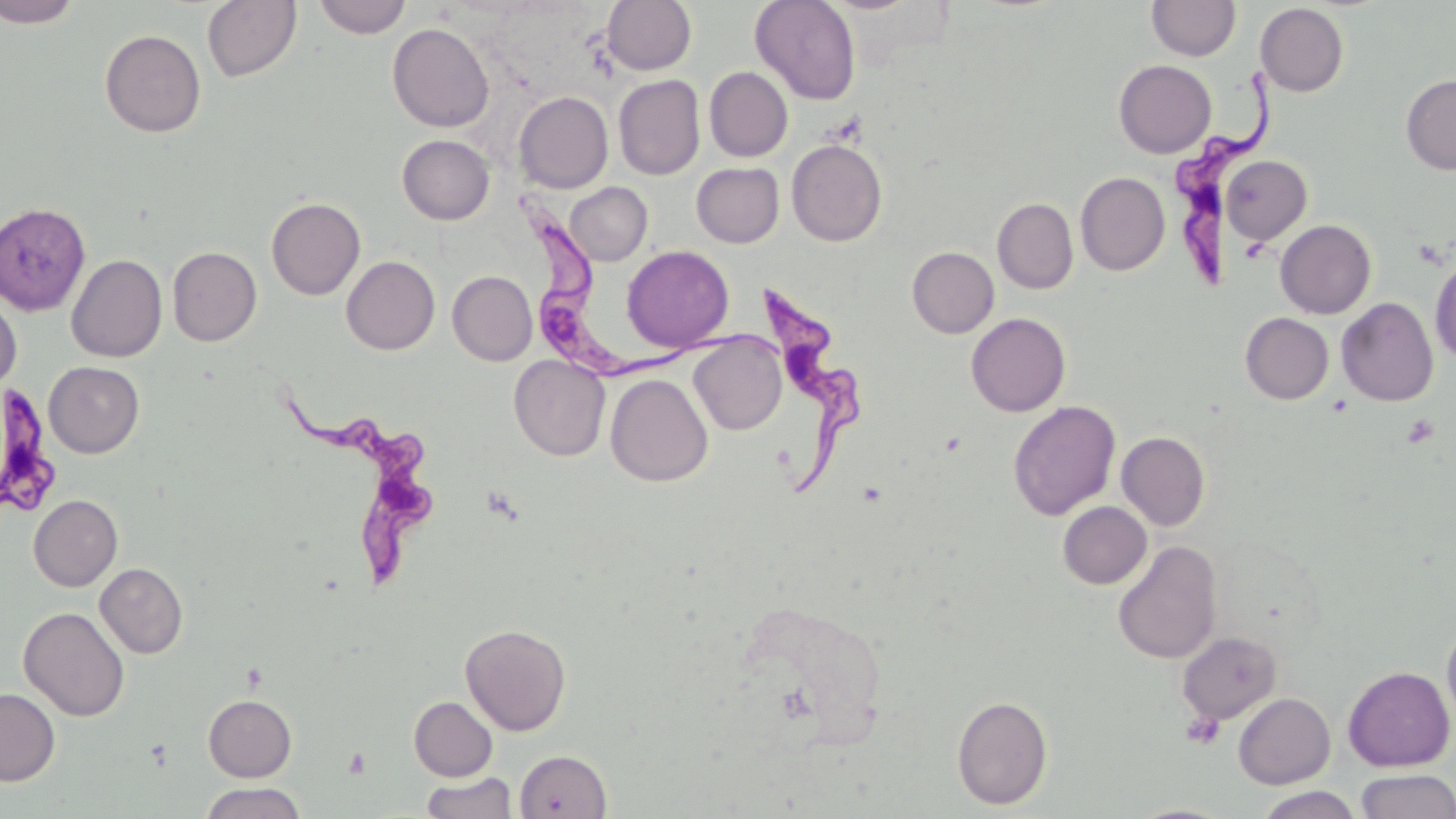

Approximate bounding boxes as [x1, y1, x2, y2] in pixels. Platelet locations: [1401, 414, 1439, 449], [1181, 711, 1223, 751], [344, 747, 371, 779]. Trypanosoma brucei locations: [1169, 73, 1284, 289], [507, 191, 689, 384], [759, 289, 873, 497], [275, 381, 453, 592], [0, 383, 63, 525]. Uninfected red blood cell locations: [1, 0, 84, 28], [312, 0, 412, 38], [601, 0, 696, 75], [749, 0, 861, 105], [201, 1, 302, 82], [1146, 1, 1240, 60], [1255, 3, 1349, 97], [387, 23, 495, 132], [99, 29, 206, 138], [1114, 60, 1216, 158], [704, 67, 793, 162], [1400, 73, 1456, 175], [613, 75, 705, 180], [514, 91, 613, 193], [397, 134, 495, 225], [787, 140, 887, 246], [1221, 155, 1312, 244], [691, 162, 785, 247], [1075, 172, 1170, 275], [565, 182, 652, 266], [266, 197, 365, 300], [993, 198, 1078, 294], [0, 203, 91, 316], [1275, 219, 1376, 319], [621, 245, 734, 353], [167, 246, 262, 346], [907, 246, 999, 338], [66, 254, 167, 362], [341, 256, 440, 355], [1430, 256, 1456, 362], [447, 271, 537, 366], [0, 290, 22, 392], [1336, 297, 1439, 406], [966, 313, 1071, 416], [1240, 313, 1333, 404], [688, 331, 787, 435], [509, 354, 610, 460], [44, 361, 144, 458], [605, 374, 713, 487], [1008, 400, 1121, 521], [1117, 431, 1211, 530], [29, 494, 122, 591], [1057, 501, 1152, 589], [1113, 540, 1223, 664], [95, 563, 188, 658], [739, 598, 891, 745], [19, 606, 130, 721], [1442, 621, 1456, 727], [460, 623, 571, 735], [1177, 631, 1282, 724], [1343, 666, 1454, 771], [0, 688, 60, 785], [1233, 693, 1335, 789], [203, 694, 297, 782], [951, 695, 1053, 810], [409, 697, 497, 781], [515, 749, 612, 818], [1355, 769, 1455, 819], [420, 772, 518, 819], [199, 783, 307, 819], [1255, 787, 1364, 819], [1125, 803, 1236, 819]. Slide-level diagnosis: Trypanosoma brucei. Image is 1456×819 pixels. May-Grünwald-Giemsa-stained preparation. One field of a larger specimen. Thin blood smear. 1000x magnification. Light microscopy.